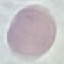
malaria status = uninfected
capture = smartphone through the microscope eyepiece
preparation = thin blood smear
stain = Giemsa
image type = automatically extracted cell patch, resized to 64 × 64 pixels